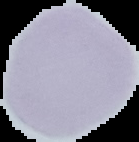

Summary:
  - Result: no Plasmodium parasites seen
  - Preparation: thin blood film
  - Image type: cell region segmented out of the field of view; surrounding area masked to black
  - Image size: 139×142 pixels